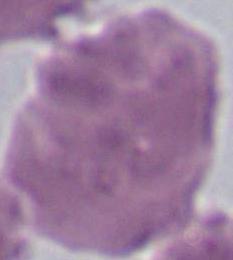

{
  "magnification": "1000x",
  "modality": "micrograph",
  "identification": "red blood cell"
}